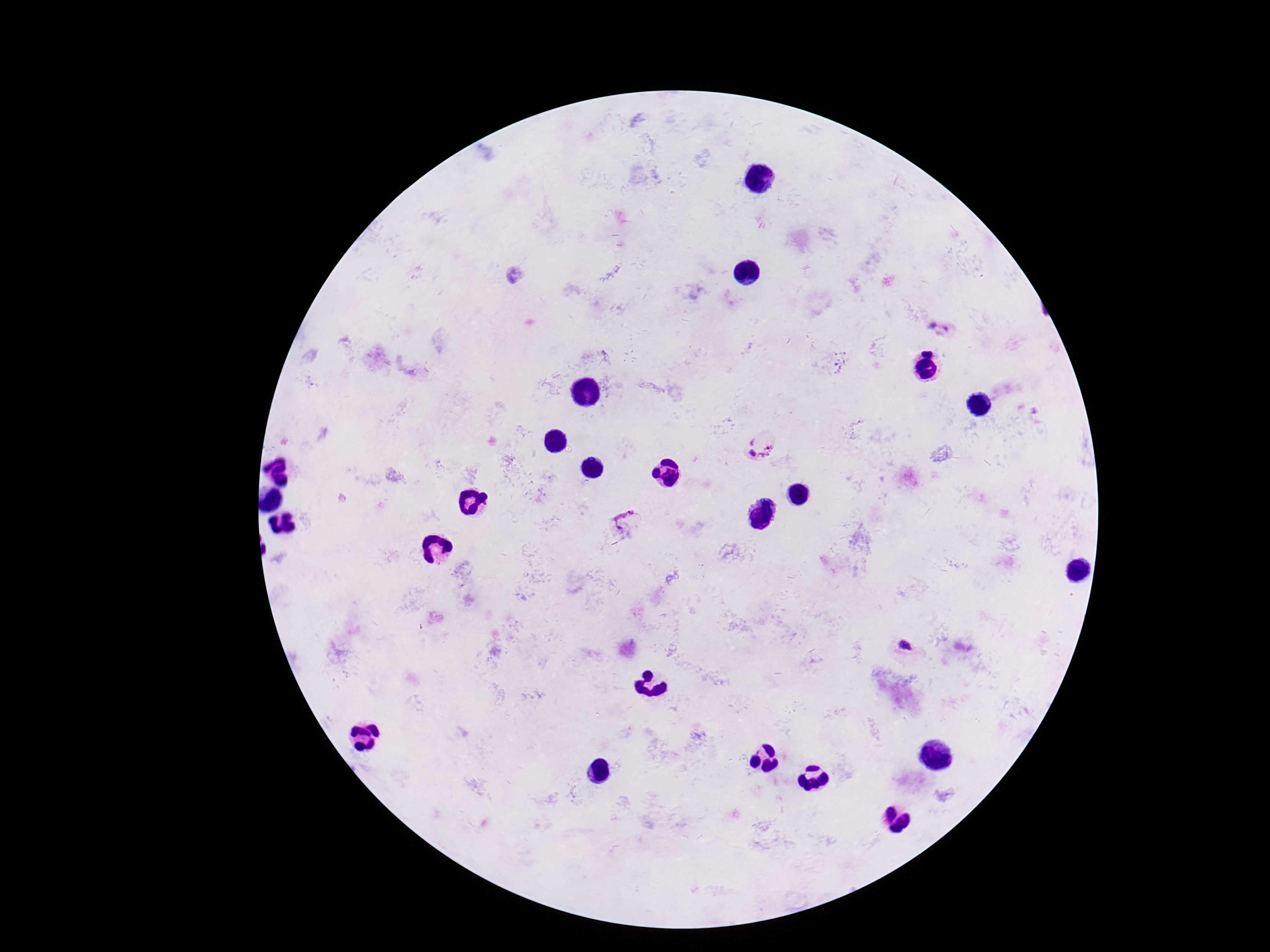
Approximate centers as [x, y] in pixels. Plasmodium parasite locations: [938, 328], [758, 444], [627, 520], [903, 646]. Giemsa stain. Image is 1270×952 pixels. Smartphone photograph taken through the microscope eyepiece. Patient malaria status: positive. Single field of view. 100x magnification. Thick blood smear.